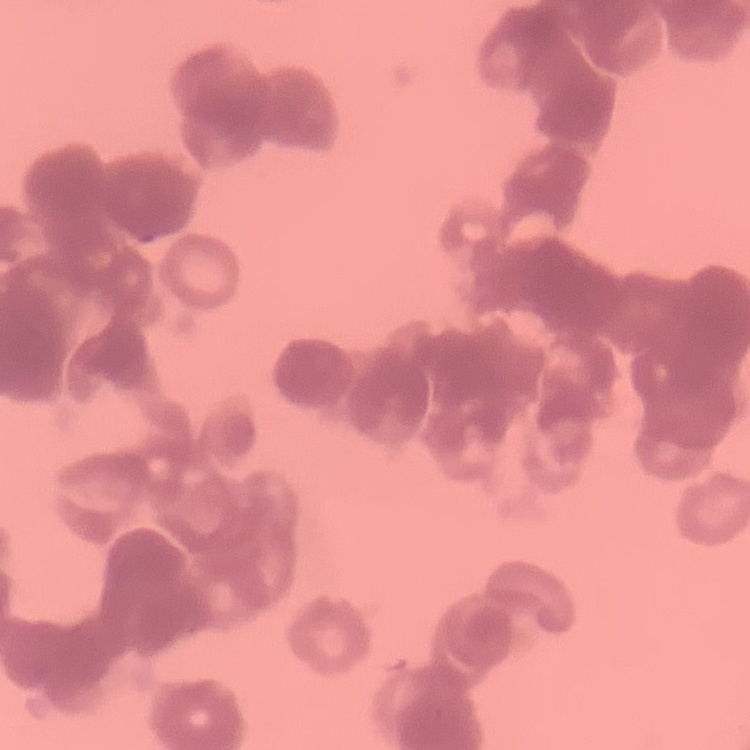

Summary:
  - Red blood cell morphology: rouleaux formation
  - Image type: square crop of a larger photomicrograph
  - Preparation: thin peripheral smear
  - Stain: Field's or Giemsa